Outline each blood parasite and name the species.
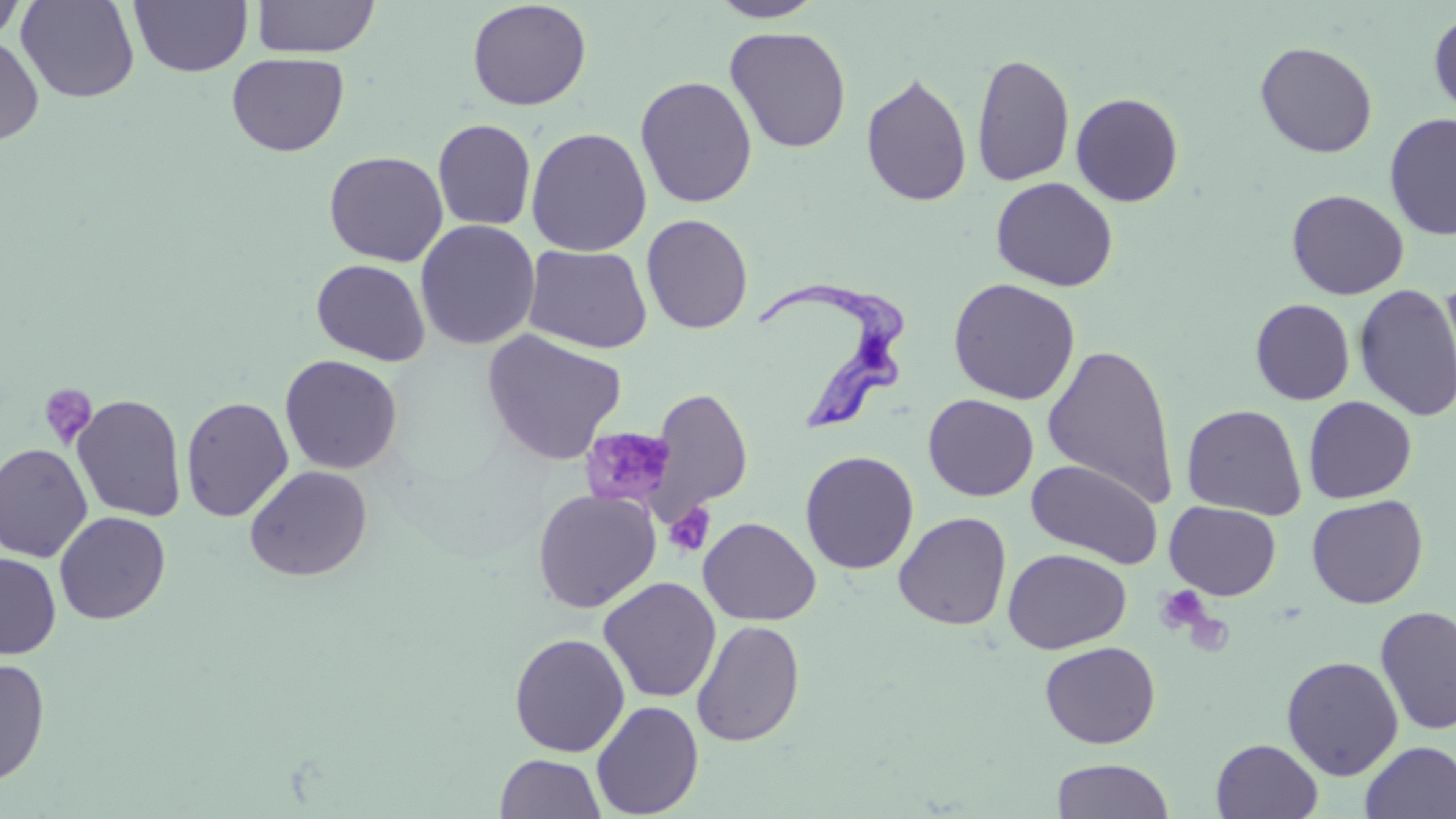
Approximate bounding boxes as named x1/y1/x2/y2 corners in pixels.
Trypanosoma brucei: (x1=756, y1=280, x2=907, y2=434).
No Plasmodium falciparum, Plasmodium ovale, Plasmodium malariae, Plasmodium vivax, or Babesia divergens observed.

Summary:
  - Uninfected red blood cell locations: (x1=16, y1=0, x2=140, y2=103), (x1=129, y1=0, x2=253, y2=77), (x1=251, y1=0, x2=380, y2=58), (x1=707, y1=0, x2=826, y2=23), (x1=0, y1=1, x2=29, y2=44), (x1=467, y1=1, x2=592, y2=111), (x1=1428, y1=9, x2=1456, y2=119), (x1=725, y1=25, x2=851, y2=153), (x1=0, y1=35, x2=44, y2=146), (x1=1255, y1=41, x2=1378, y2=157), (x1=227, y1=52, x2=349, y2=157), (x1=970, y1=52, x2=1075, y2=187), (x1=860, y1=71, x2=972, y2=207), (x1=635, y1=75, x2=758, y2=208), (x1=1070, y1=92, x2=1184, y2=207), (x1=1384, y1=112, x2=1456, y2=240), (x1=433, y1=119, x2=536, y2=231), (x1=526, y1=127, x2=652, y2=256), (x1=324, y1=151, x2=448, y2=266), (x1=991, y1=177, x2=1118, y2=292), (x1=1287, y1=189, x2=1409, y2=300), (x1=641, y1=214, x2=753, y2=334), (x1=415, y1=219, x2=540, y2=351), (x1=523, y1=244, x2=652, y2=354), (x1=311, y1=258, x2=430, y2=366), (x1=948, y1=277, x2=1081, y2=405), (x1=1437, y1=277, x2=1456, y2=407), (x1=1354, y1=284, x2=1456, y2=421), (x1=1250, y1=299, x2=1355, y2=405), (x1=480, y1=329, x2=627, y2=466), (x1=1042, y1=342, x2=1179, y2=506), (x1=279, y1=354, x2=403, y2=474), (x1=645, y1=387, x2=753, y2=522), (x1=72, y1=394, x2=188, y2=523), (x1=923, y1=394, x2=1039, y2=501), (x1=180, y1=396, x2=294, y2=522), (x1=1303, y1=396, x2=1417, y2=503), (x1=1181, y1=404, x2=1307, y2=520), (x1=0, y1=443, x2=93, y2=562), (x1=800, y1=450, x2=920, y2=575), (x1=1027, y1=459, x2=1163, y2=568), (x1=244, y1=465, x2=373, y2=581), (x1=532, y1=489, x2=660, y2=613), (x1=1306, y1=494, x2=1428, y2=608), (x1=1165, y1=501, x2=1281, y2=600), (x1=54, y1=511, x2=171, y2=625), (x1=893, y1=511, x2=1012, y2=630), (x1=699, y1=517, x2=821, y2=626), (x1=1003, y1=548, x2=1131, y2=654), (x1=0, y1=553, x2=61, y2=660), (x1=598, y1=577, x2=722, y2=703), (x1=1375, y1=605, x2=1456, y2=735), (x1=691, y1=619, x2=806, y2=746), (x1=509, y1=632, x2=631, y2=757), (x1=1039, y1=641, x2=1161, y2=749), (x1=1281, y1=655, x2=1404, y2=780), (x1=0, y1=657, x2=51, y2=786), (x1=591, y1=700, x2=704, y2=818), (x1=1211, y1=738, x2=1323, y2=819), (x1=1359, y1=740, x2=1456, y2=819), (x1=494, y1=753, x2=606, y2=818), (x1=1051, y1=758, x2=1175, y2=818)
  - Platelet locations: (x1=38, y1=383, x2=98, y2=449), (x1=580, y1=426, x2=680, y2=515), (x1=664, y1=502, x2=716, y2=557), (x1=1155, y1=585, x2=1212, y2=636)
  - Slide-level diagnosis: Trypanosoma brucei
  - Field of view: one of a larger specimen
  - Modality: light microscopy
  - Preparation: thin blood film
  - Magnification: 1000x
  - Stain: May-Grünwald-Giemsa
  - Image size: 1456×819 pixels